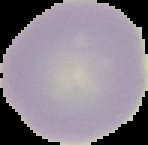

Summary:
  - Image size: 148×145 pixels
  - Image type: cell region segmented out of the field of view; surrounding area masked to black
  - Malaria status: uninfected
  - Preparation: thin blood film